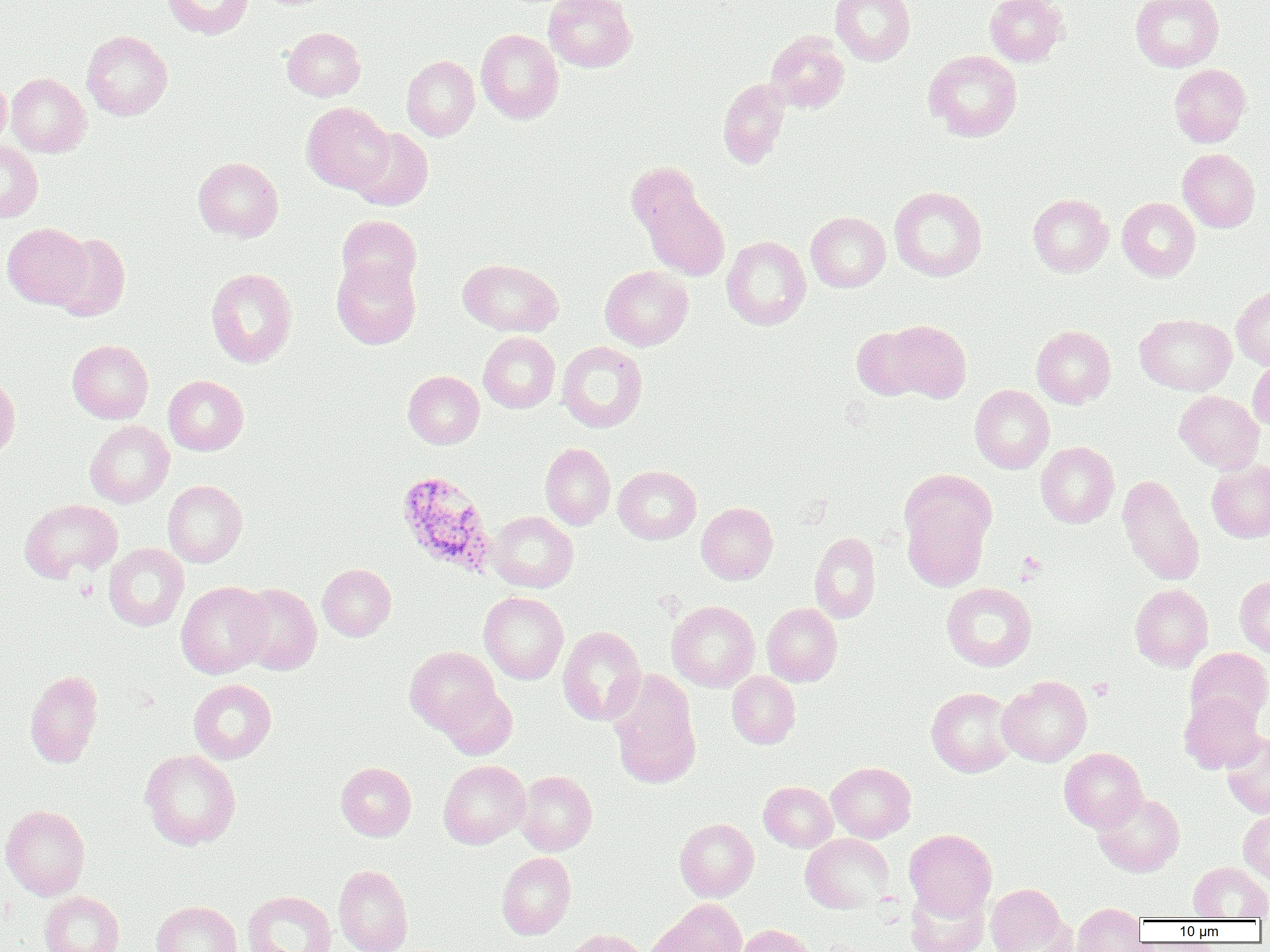
Summary:
  - Coordinate format: approximate bounding boxes as (x1,y1)-(x2,y2) corner pairs in pixels
  - Uninfected red blood cell locations: (162,0)-(254,39), (544,0)-(637,72), (831,0)-(915,65), (984,0)-(1067,66), (1131,0)-(1223,72), (282,27)-(365,101), (476,29)-(564,123), (82,30)-(172,120), (765,31)-(850,113), (924,50)-(1022,141), (401,55)-(480,140), (1169,64)-(1251,147), (5,73)-(91,157), (0,75)-(11,151), (718,78)-(790,167), (302,102)-(394,193), (348,128)-(433,210), (0,140)-(43,222), (1178,149)-(1260,232), (193,157)-(283,241), (625,162)-(704,237), (889,186)-(987,281), (640,191)-(730,280), (1028,193)-(1113,276), (1117,197)-(1200,280), (806,212)-(890,292), (336,214)-(422,296), (2,222)-(91,308), (50,233)-(131,320), (722,236)-(811,330), (331,257)-(421,349), (458,259)-(563,337), (600,266)-(693,350), (206,268)-(297,368), (1232,285)-(1270,369), (1135,313)-(1237,395), (885,320)-(971,401), (1031,325)-(1116,408), (851,326)-(930,400), (478,332)-(560,413), (67,339)-(154,423), (557,341)-(647,432), (1248,358)-(1270,432), (403,371)-(484,449), (0,375)-(20,462), (163,375)-(248,455), (970,385)-(1054,473), (1174,391)-(1264,473), (85,420)-(174,508), (1035,442)-(1119,528), (541,443)-(615,530), (1207,459)-(1270,542), (613,465)-(701,544), (898,469)-(996,554), (1117,475)-(1204,584), (163,480)-(247,567), (20,499)-(123,582), (697,502)-(778,584), (902,504)-(989,591), (489,511)-(578,592), (809,531)-(881,623), (104,543)-(189,631), (317,564)-(396,640), (1235,576)-(1270,656), (176,581)-(271,679), (941,582)-(1038,671), (234,583)-(321,675), (1130,583)-(1213,671), (479,592)-(568,684), (667,600)-(760,691), (762,602)-(842,686), (558,626)-(646,725), (405,646)-(499,733), (1186,647)-(1270,729), (607,669)-(702,789), (25,670)-(103,768), (726,671)-(800,749), (997,675)-(1092,766), (188,678)-(277,763), (437,684)-(517,759), (926,687)-(1017,777), (1179,692)-(1265,773), (1221,731)-(1270,818), (1059,747)-(1147,832), (139,749)-(241,850), (439,759)-(530,848), (335,762)-(416,841), (826,762)-(916,842), (516,770)-(597,855), (759,781)-(837,852), (1093,792)-(1184,876), (1,804)-(90,900), (1239,810)-(1270,884), (675,818)-(759,901), (904,828)-(997,918), (800,833)-(894,913), (497,852)-(576,940), (1188,861)-(1270,920), (333,864)-(413,952), (985,883)-(1069,951), (904,884)-(990,952), (242,890)-(337,952), (40,891)-(124,952), (653,899)-(747,952), (152,900)-(241,952), (1073,903)-(1146,952), (736,924)-(817,952), (562,928)-(648,952)
  - Plasmodium ovale-infected red blood cell locations: (396,470)-(498,578)
  - Platelet locations: (1017,551)-(1046,580), (1088,678)-(1114,700)
  - Slide-level diagnosis: Plasmodium ovale
  - Image size: 1270×952 pixels
  - Preparation: thin blood smear
  - Magnification: 1000x
  - Field of view: one of a larger specimen
  - Modality: light microscopy